Assess the morphology of the red blood cells.
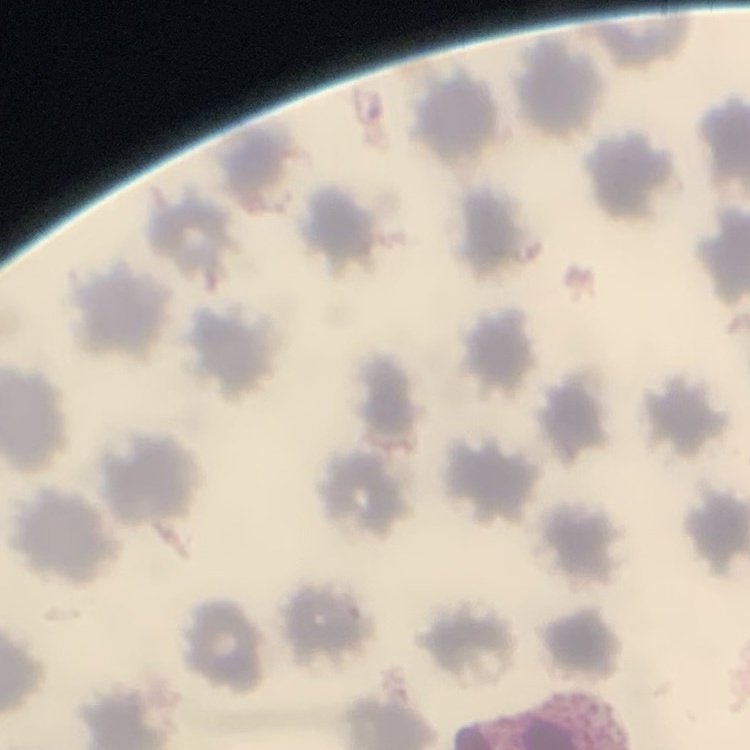
They show no rouleaux formation.

Summary:
  - Image type: square crop of a larger photomicrograph
  - Preparation: thin peripheral smear
  - Stain: Field's or Giemsa